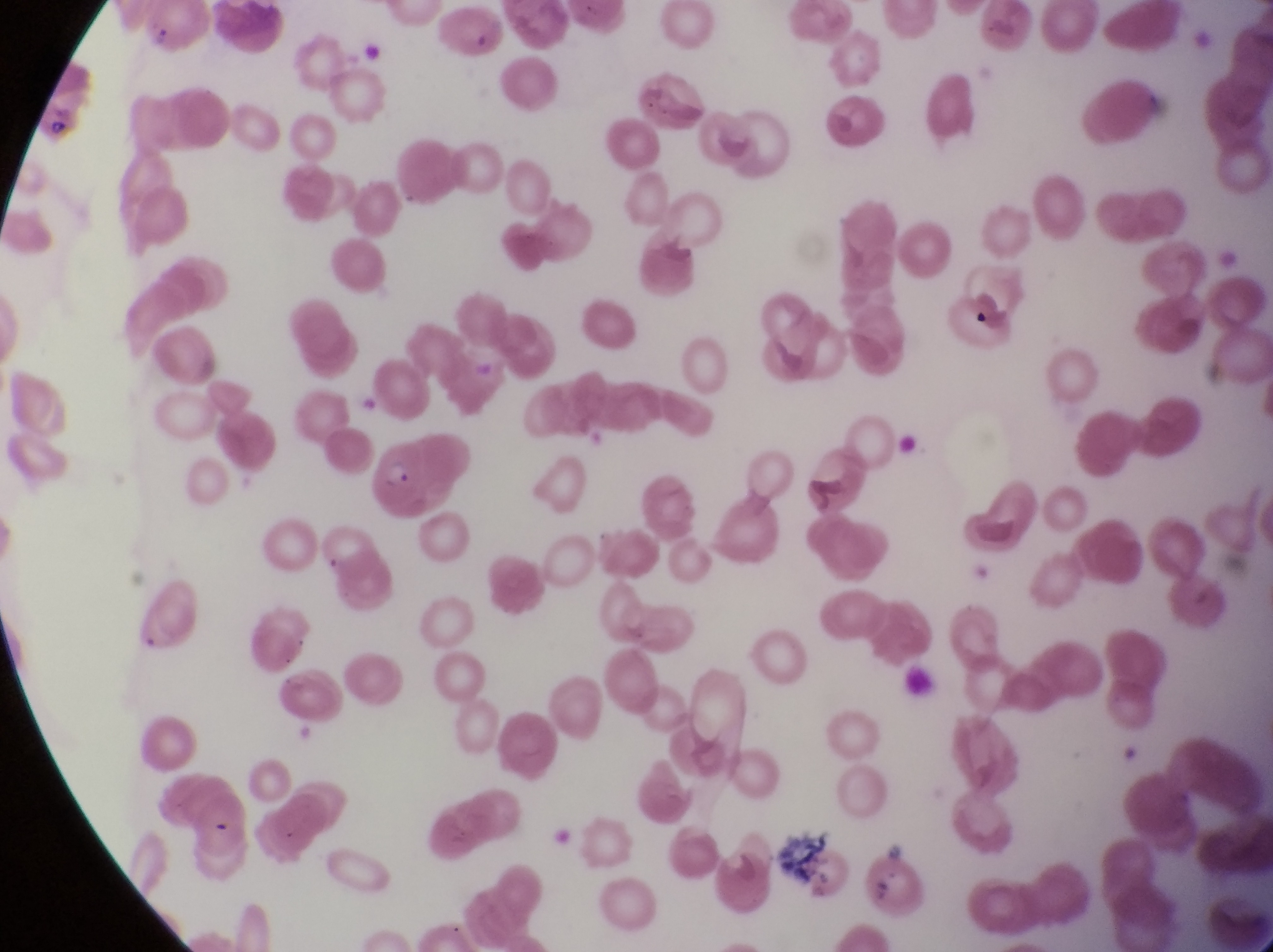

magnification = 1000x
field of view = single
country = Uganda
capture = smartphone photograph through the eyepiece of an Olympus CX-23 microscope
parasitised red blood cell locations = approximate bounding boxes as [left, top, right, bottom] in pixels: [370, 440, 445, 527], [314, 521, 379, 583]
image size = 1273×952 pixels
preparation = thin blood film